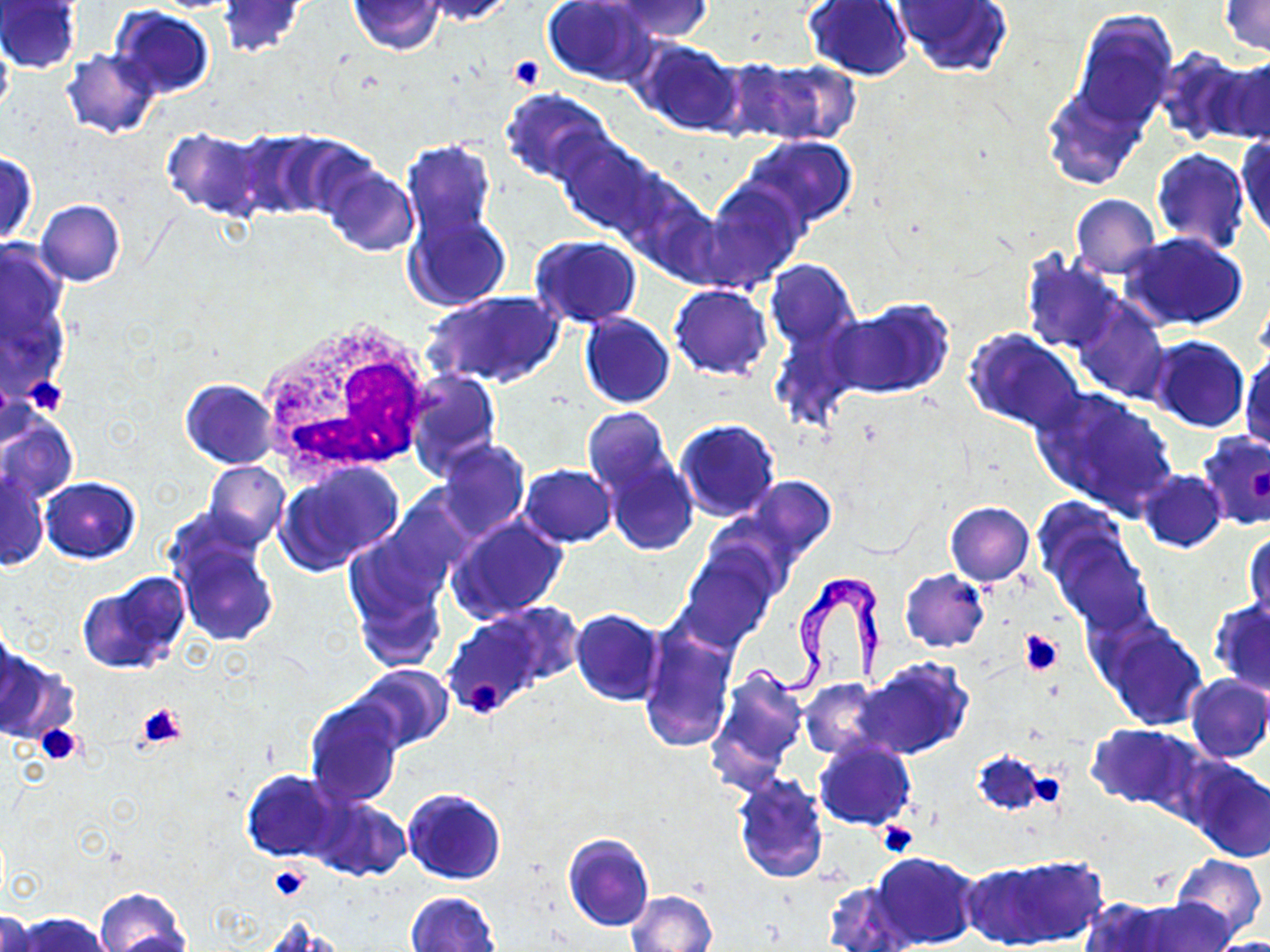

Approximate bounding boxes as (x1, y1, x2, y2) in pixels. Platelet locations: (509, 56, 544, 92), (23, 376, 69, 416), (1017, 629, 1063, 677), (468, 682, 503, 713), (137, 702, 187, 750), (34, 723, 82, 765), (1023, 769, 1066, 807), (877, 820, 919, 858), (270, 864, 311, 901). Trypanosoma brucei locations: (745, 571, 883, 693). White blood cell locations: (257, 317, 434, 481). Uninfected red blood cell locations: (1, 0, 83, 72), (418, 0, 518, 24), (541, 0, 657, 87), (606, 0, 713, 40), (217, 1, 307, 58), (347, 1, 446, 56), (804, 1, 915, 82), (896, 1, 1011, 78), (1218, 1, 1270, 57), (109, 6, 214, 99), (1069, 10, 1180, 129), (0, 33, 13, 123), (634, 39, 744, 136), (61, 49, 163, 139), (1155, 49, 1261, 146), (1210, 53, 1270, 147), (738, 57, 861, 146), (1042, 85, 1149, 188), (500, 89, 613, 184), (162, 128, 265, 218), (225, 130, 347, 218), (552, 132, 666, 240), (1236, 134, 1269, 247), (741, 136, 857, 229), (401, 139, 499, 248), (1151, 148, 1249, 254), (0, 152, 37, 244), (321, 165, 420, 257), (614, 171, 719, 279), (701, 181, 805, 288), (1070, 194, 1160, 277), (36, 199, 126, 286), (404, 209, 510, 313), (1121, 232, 1248, 331), (530, 235, 641, 327), (1, 242, 69, 398), (1020, 248, 1126, 355), (766, 259, 859, 352), (669, 284, 773, 378), (424, 290, 562, 390), (1073, 298, 1169, 404), (830, 300, 954, 400), (579, 313, 676, 409), (770, 320, 859, 433), (963, 328, 1086, 434), (1150, 336, 1250, 433), (1240, 347, 1269, 452), (406, 369, 502, 474), (181, 379, 278, 468), (1030, 386, 1179, 519), (581, 406, 674, 496), (0, 414, 78, 505), (674, 420, 779, 523), (1197, 434, 1270, 531), (435, 439, 530, 539), (601, 451, 700, 556), (204, 461, 289, 550), (277, 462, 403, 573), (518, 464, 615, 547), (1, 469, 48, 571), (1138, 470, 1227, 553), (736, 477, 837, 572), (41, 478, 140, 562), (945, 501, 1034, 586), (1041, 507, 1154, 634), (448, 514, 567, 621), (168, 524, 279, 649), (1246, 527, 1269, 624), (345, 537, 449, 670), (681, 550, 776, 652), (899, 569, 990, 652), (78, 571, 191, 676), (1208, 599, 1270, 694), (489, 602, 584, 686), (570, 609, 664, 706), (441, 611, 549, 718), (1096, 619, 1208, 730), (639, 626, 735, 753), (0, 649, 74, 745), (855, 656, 974, 760), (353, 664, 452, 751), (706, 665, 809, 792), (1184, 674, 1270, 764), (800, 678, 883, 760), (303, 696, 406, 808), (1088, 724, 1196, 807), (814, 738, 916, 830), (973, 751, 1050, 816), (1182, 757, 1270, 862), (241, 769, 341, 861), (733, 774, 828, 883), (402, 788, 506, 885), (305, 794, 411, 883), (562, 832, 654, 931), (872, 852, 981, 949), (1169, 854, 1267, 943), (969, 855, 1104, 949), (823, 881, 916, 952), (95, 888, 190, 952), (627, 890, 717, 952), (405, 891, 501, 952), (1079, 896, 1182, 952), (1125, 897, 1236, 951), (0, 909, 44, 951), (12, 913, 112, 952), (260, 918, 340, 952), (1205, 936, 1270, 952). Slide-level diagnosis: Trypanosoma brucei. One field of a larger specimen. Image is 1270×952 pixels. May-Grünwald-Giemsa-stained preparation. 1000x magnification. Optical microscopy. Thin blood film.